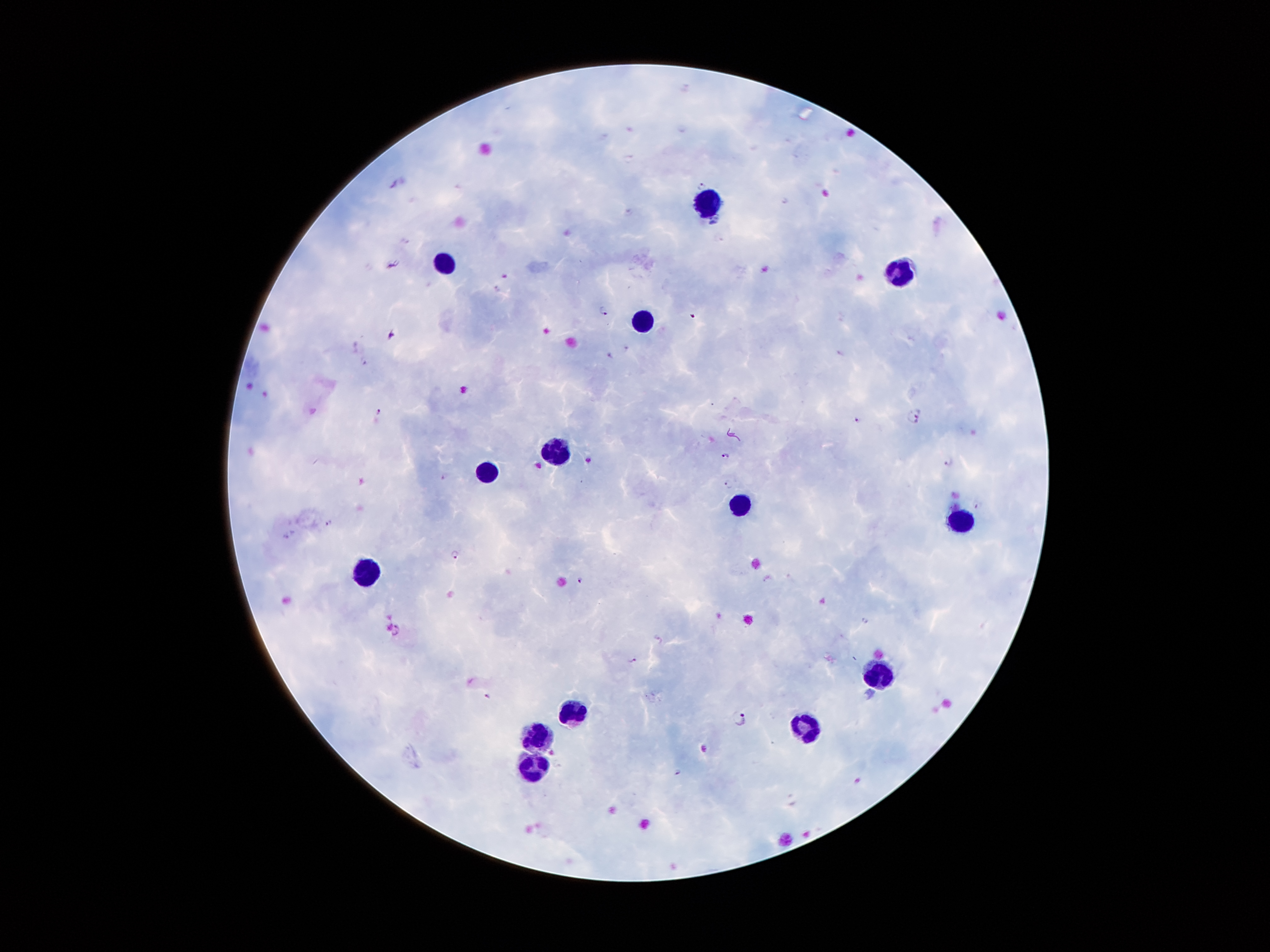 Approximate centers as [x, y] in pixels. Leukocyte locations: [706, 201], [444, 264], [900, 275], [643, 320], [554, 449], [489, 473], [737, 504], [961, 523], [366, 574], [878, 675], [572, 711], [811, 724], [538, 737], [534, 767]. Plasmodium parasite locations: [701, 186], [786, 200], [392, 263], [603, 310], [392, 335], [626, 348], [609, 356], [363, 361], [377, 411], [915, 415], [857, 419], [726, 456], [951, 463], [443, 476], [729, 483], [978, 506], [329, 523], [456, 554], [580, 580], [398, 631], [634, 660], [488, 696], [738, 719], [677, 771]. Thick blood film. Single field of view. Giemsa-stained preparation. Patient malaria status: positive for Plasmodium falciparum. Image is 1270×952 pixels. 100x magnification. Photographed through the microscope eyepiece with a smartphone camera.